Comment on the morphology of the erythrocytes.
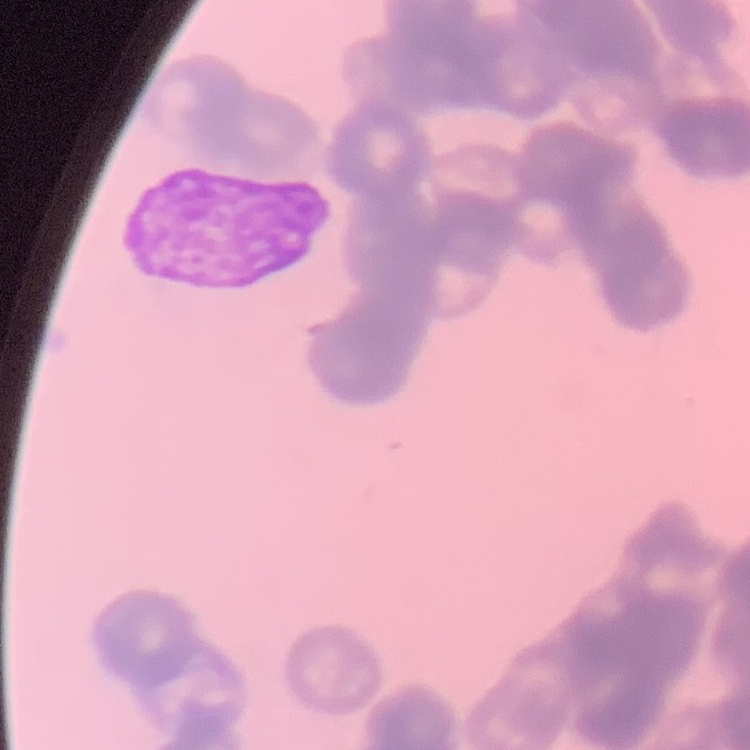
They show rouleaux formation.

Summary:
  - Preparation: thin peripheral smear
  - Image type: one tile cut from a larger photomicrograph
  - Stain: Field's or Giemsa